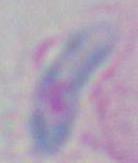

Summary:
  - Identification: Toxoplasma gondii
  - Magnification: 1000x
  - Modality: micrograph